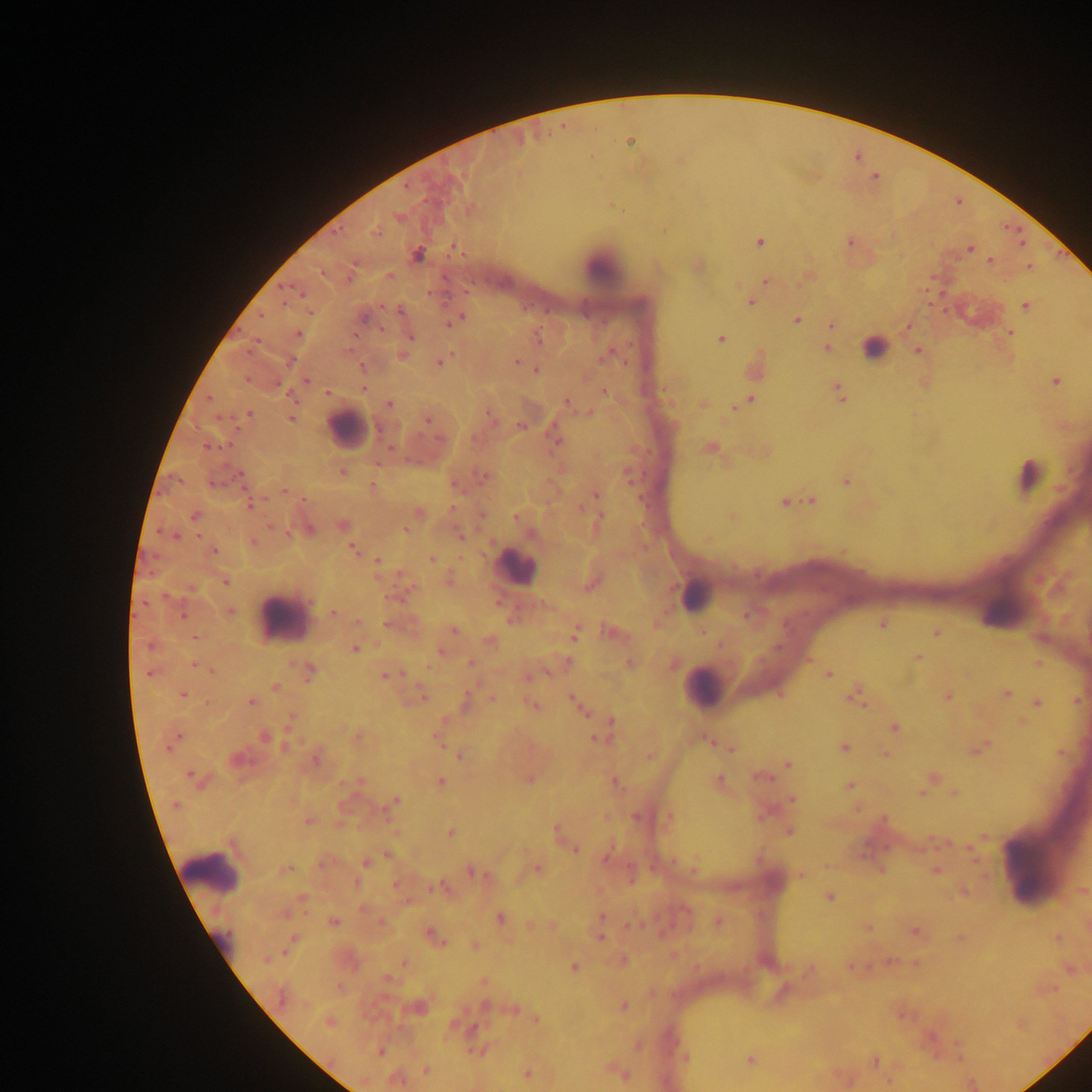 Approximate centers as [x, y] in pixels. Leukocyte locations: [601, 266], [875, 348], [347, 429], [1027, 474], [514, 567], [695, 595], [282, 617], [704, 687], [1034, 862], [210, 872]. Plasmodium parasite locations: [630, 141], [398, 217], [376, 231], [849, 241], [1020, 241], [759, 242], [971, 248], [417, 255], [990, 260], [697, 265], [1029, 266], [389, 275], [806, 276], [765, 280], [750, 302], [1025, 305], [459, 318], [796, 319], [451, 320], [831, 324], [907, 326], [1009, 332], [298, 333], [409, 336], [719, 338], [537, 339], [827, 347], [917, 351], [402, 355], [606, 355], [439, 361], [516, 362], [362, 368], [536, 370], [306, 381], [1054, 381], [362, 387], [603, 391], [839, 392], [327, 393], [749, 400], [566, 403], [388, 404], [703, 404], [735, 406], [248, 414], [490, 415], [290, 417], [427, 419], [520, 426], [555, 438], [710, 448], [342, 472], [627, 474], [240, 476], [483, 477], [845, 480], [371, 486], [284, 490], [595, 494], [800, 500], [784, 501], [810, 501], [250, 504], [418, 513], [195, 515], [515, 517], [599, 517], [732, 517], [342, 525], [271, 527], [307, 529], [405, 529], [460, 534], [174, 536], [708, 539], [253, 542], [352, 548], [213, 550], [431, 558], [377, 561], [448, 578], [224, 581], [592, 584], [228, 612], [333, 613], [747, 615], [357, 621], [656, 623], [881, 623], [390, 624], [452, 630], [610, 631], [702, 631], [575, 632], [936, 632], [195, 638], [489, 641], [152, 645], [355, 648], [440, 651], [918, 656], [568, 661], [470, 663], [629, 663], [1038, 663], [672, 664], [195, 665], [308, 672], [149, 673], [828, 674], [387, 675], [528, 675], [275, 687], [1005, 693], [182, 694], [421, 695], [854, 695], [947, 697], [492, 699], [1075, 699], [250, 701], [575, 701], [465, 702], [1036, 703], [532, 705], [580, 708], [291, 719], [611, 721], [893, 726], [264, 737], [356, 737], [599, 737], [707, 738], [438, 739], [173, 740], [843, 748], [977, 748], [731, 749], [1060, 752], [884, 754], [459, 756], [649, 756], [316, 758], [238, 760], [788, 764], [760, 776], [194, 777], [932, 777], [528, 779], [360, 781], [439, 781], [614, 781], [719, 781], [848, 786], [851, 789], [953, 792], [922, 793], [791, 799], [394, 801], [856, 808], [605, 816], [636, 816], [668, 816], [307, 821], [555, 830], [788, 830], [451, 833], [983, 836], [945, 842], [574, 849], [971, 850], [387, 854], [606, 858], [974, 859], [322, 863], [365, 863], [694, 865], [284, 869], [537, 869], [880, 869], [935, 870], [472, 872], [630, 875], [801, 875], [395, 885], [442, 887], [1082, 890], [964, 891], [828, 897], [301, 899], [363, 908], [284, 913], [601, 917], [499, 918], [717, 921], [333, 922], [381, 923], [531, 924], [553, 925], [634, 925], [867, 927], [914, 931], [434, 937], [599, 937], [958, 937], [1057, 938], [291, 943], [474, 946], [673, 955], [268, 958], [621, 960], [888, 961], [404, 963], [914, 963], [850, 966], [572, 968], [809, 969], [1069, 969], [387, 980], [483, 982], [338, 987], [418, 1006], [485, 1006], [622, 1006], [512, 1009], [535, 1019], [329, 1022], [637, 1044], [379, 1051], [685, 1057], [749, 1059], [874, 1060], [611, 1068], [425, 1070], [618, 1071], [526, 1073], [624, 1075], [396, 1079], [888, 1081]. Collected in Ghana. Photographed through a microscope with a mobile-phone camera. Image is 1092×1092 pixels. Single field of view. Thick blood smear.